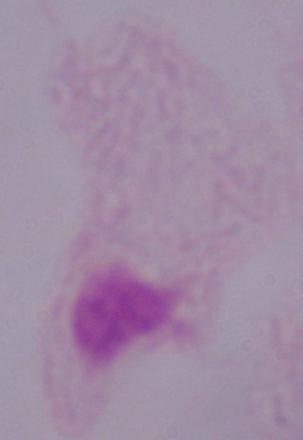

Summary:
  - Identification: trichomonad
  - Magnification: 1000x
  - Modality: photomicrograph